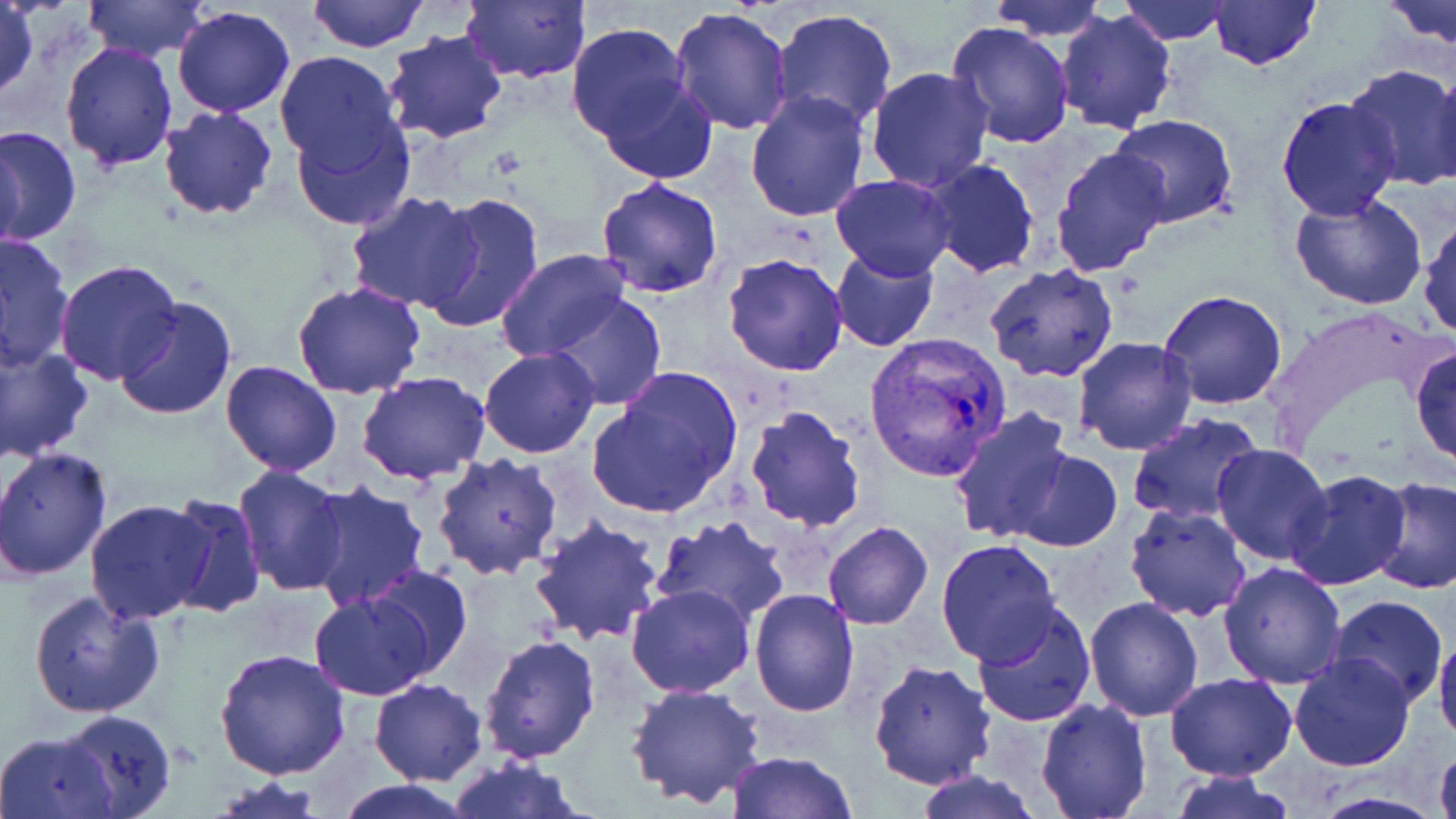
Approximate bounding boxes as (x1, y1, x2, y2) in pixels. Uninfected red blood cell locations: (307, 0, 431, 51), (461, 0, 590, 84), (984, 0, 1113, 41), (1116, 0, 1234, 45), (1380, 0, 1456, 55), (83, 1, 209, 61), (1208, 1, 1322, 71), (1, 2, 38, 102), (172, 5, 295, 117), (669, 6, 796, 135), (1054, 8, 1178, 133), (770, 9, 899, 131), (946, 22, 1075, 150), (566, 24, 691, 141), (383, 31, 509, 145), (58, 43, 179, 170), (273, 52, 403, 173), (1428, 61, 1456, 194), (1342, 65, 1456, 191), (866, 66, 995, 192), (597, 75, 718, 184), (745, 91, 872, 224), (1275, 96, 1401, 221), (157, 106, 279, 221), (291, 111, 415, 230), (1107, 113, 1239, 228), (0, 126, 82, 247), (1, 133, 26, 258), (1050, 145, 1173, 276), (920, 159, 1039, 280), (830, 174, 956, 281), (595, 178, 725, 298), (347, 193, 480, 312), (421, 193, 544, 335), (1290, 194, 1429, 311), (1418, 214, 1456, 340), (1, 233, 73, 370), (830, 249, 938, 351), (496, 250, 631, 363), (722, 251, 852, 376), (55, 260, 184, 385), (983, 266, 1120, 385), (292, 281, 425, 401), (1160, 290, 1288, 410), (548, 292, 668, 411), (114, 297, 238, 420), (1073, 338, 1198, 456), (0, 343, 93, 462), (1410, 343, 1456, 468), (479, 347, 599, 460), (221, 360, 343, 475), (588, 369, 741, 520), (358, 371, 491, 485), (745, 405, 867, 533), (948, 406, 1075, 541), (1127, 413, 1266, 526), (1211, 444, 1333, 564), (0, 447, 112, 582), (1010, 450, 1123, 552), (432, 451, 563, 580), (232, 464, 348, 595), (1284, 468, 1412, 590), (1370, 477, 1456, 595), (304, 481, 432, 611), (162, 492, 265, 618), (84, 500, 217, 623), (1124, 504, 1253, 621), (651, 515, 792, 624), (530, 516, 666, 646), (823, 521, 932, 630), (936, 538, 1063, 666), (1218, 561, 1347, 687), (364, 566, 471, 678), (625, 585, 754, 699), (750, 588, 861, 717), (28, 590, 165, 718), (307, 590, 439, 700), (1327, 595, 1448, 708), (1083, 596, 1204, 720), (972, 601, 1097, 728), (1433, 631, 1456, 750), (478, 632, 601, 762), (214, 647, 351, 778), (1290, 654, 1416, 771), (870, 659, 996, 790), (1164, 672, 1296, 781), (369, 677, 487, 786), (626, 682, 769, 809), (1035, 698, 1152, 819), (57, 708, 176, 818), (0, 731, 115, 818), (1434, 743, 1456, 819), (727, 750, 859, 819), (447, 757, 587, 819), (912, 768, 1044, 819), (1165, 772, 1302, 819), (331, 779, 483, 818). Plasmodium vivax-infected red blood cell locations: (863, 331, 1013, 480). Slide-level diagnosis: Plasmodium vivax. 1000x magnification. One field of a larger specimen. Thin blood smear. Image is 1456×819 pixels. Optical microscopy. May-Grünwald-Giemsa-stained preparation.